Report the malaria status of this cell.
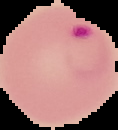
Parasitized.

From a thin blood film. Image is 118×130 pixels. Segmented cell region on a black background.